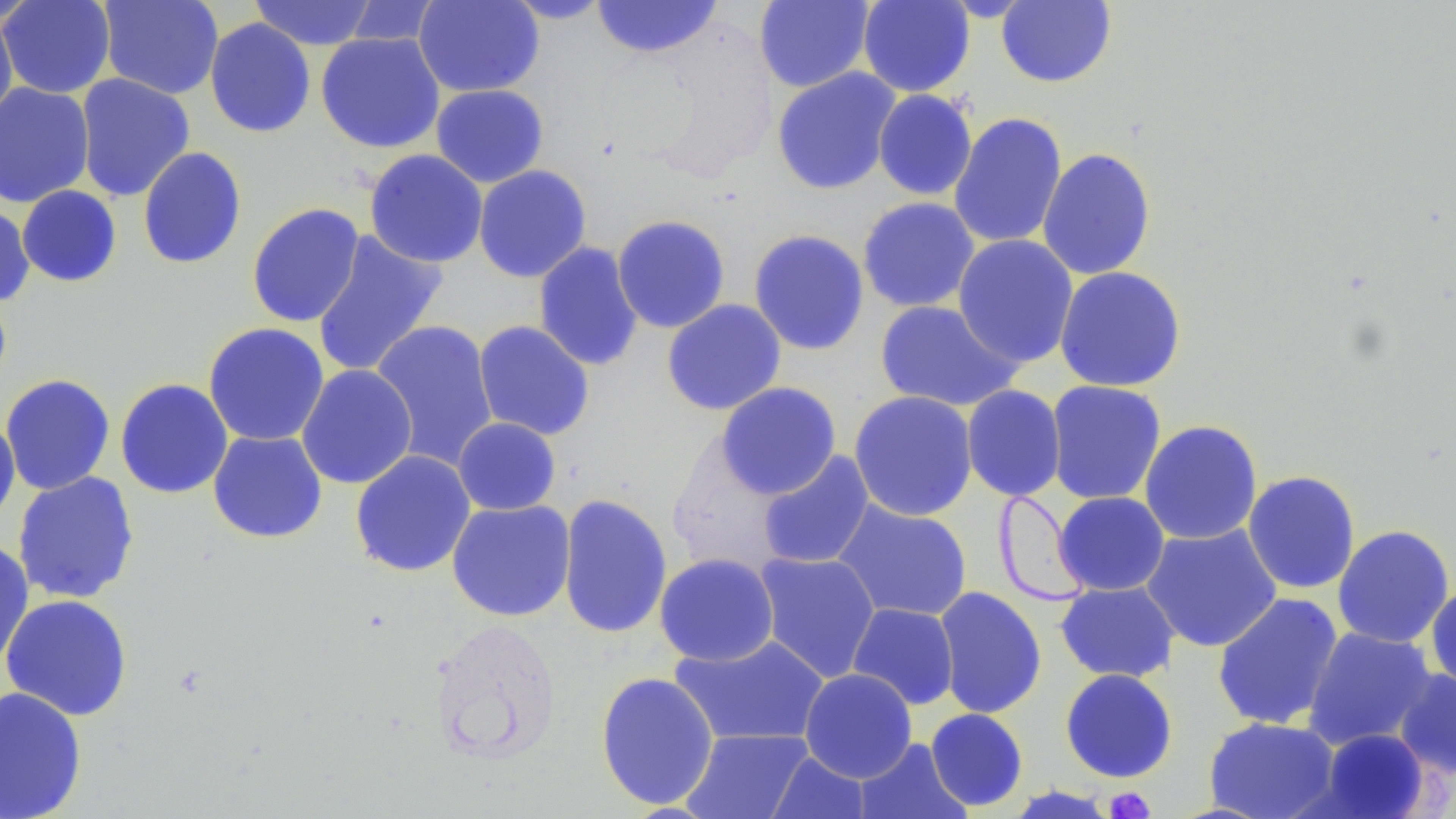
Approximate bounding boxes as (x1, y1, x2, y2) in pixels. Uninfected red blood cell locations: (0, 0, 42, 29), (1, 0, 115, 99), (97, 0, 224, 100), (248, 0, 379, 50), (413, 0, 544, 97), (502, 0, 615, 24), (591, 0, 721, 59), (754, 0, 874, 92), (858, 0, 975, 97), (997, 0, 1116, 88), (341, 1, 443, 47), (0, 9, 18, 128), (204, 17, 316, 138), (315, 32, 446, 153), (771, 67, 902, 195), (75, 73, 195, 202), (0, 81, 95, 208), (430, 84, 548, 187), (872, 89, 977, 201), (948, 112, 1067, 249), (137, 147, 247, 269), (1037, 147, 1157, 280), (364, 149, 488, 268), (473, 164, 592, 282), (17, 185, 122, 287), (857, 197, 980, 313), (0, 202, 35, 307), (246, 202, 365, 328), (611, 214, 731, 333), (748, 229, 870, 356), (311, 230, 449, 378), (952, 234, 1079, 368), (533, 241, 645, 372), (1053, 265, 1187, 392), (661, 299, 787, 416), (875, 300, 1024, 411), (368, 320, 500, 470), (472, 320, 595, 440), (203, 322, 330, 446), (296, 364, 418, 489), (0, 374, 116, 495), (115, 378, 233, 499), (1045, 380, 1166, 505), (715, 381, 842, 499), (961, 385, 1067, 502), (848, 390, 978, 521), (0, 413, 20, 531), (452, 417, 561, 516), (1139, 419, 1263, 545), (207, 429, 328, 544), (350, 450, 476, 577), (757, 450, 875, 569), (1242, 470, 1361, 594), (12, 471, 140, 604), (994, 489, 1095, 605), (1053, 491, 1170, 596), (557, 493, 672, 640), (447, 499, 576, 622), (831, 499, 973, 622), (1141, 523, 1282, 652), (1333, 524, 1455, 649), (0, 538, 35, 673), (754, 551, 881, 683), (654, 552, 779, 665), (1426, 580, 1456, 694), (1054, 581, 1180, 683), (933, 586, 1047, 719), (1212, 592, 1344, 731), (0, 594, 134, 721), (846, 603, 960, 710), (430, 617, 564, 766), (1303, 626, 1436, 750), (669, 633, 831, 747), (799, 667, 918, 782), (1059, 667, 1178, 783), (1393, 668, 1456, 779), (595, 671, 719, 810), (0, 686, 87, 819), (925, 708, 1029, 811), (1204, 717, 1340, 819), (682, 728, 813, 818), (1316, 728, 1432, 818), (852, 737, 972, 819), (766, 751, 872, 818), (1001, 784, 1122, 818). Platelet locations: (1104, 787, 1156, 818). Slide-level diagnosis: no evidence of blood parasites. Single field of view. Image is 1456×819 pixels. Optical microscopy. May-Grünwald-Giemsa stain. 1000x magnification. Thin blood smear.